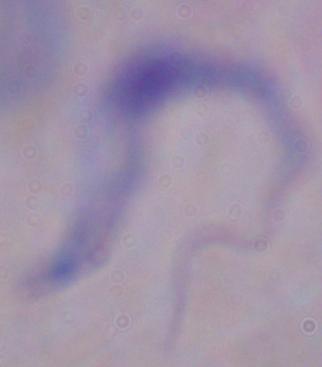
Summary:
  - Magnification: 1000x
  - Identification: trypanosome
  - Modality: photomicrograph